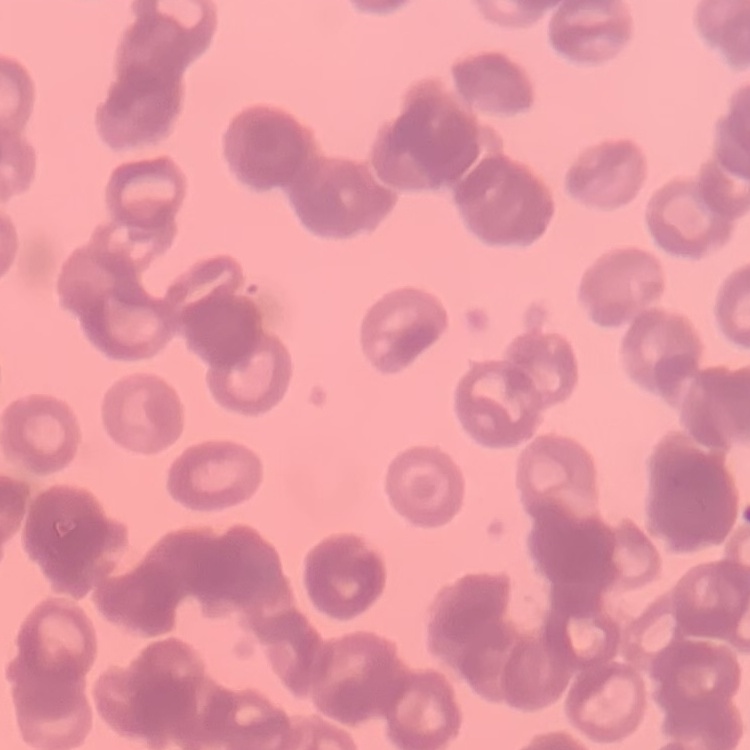

Summary:
  - Red blood cell morphology: rouleaux formation
  - Preparation: thin blood film
  - Image type: square crop of a larger photomicrograph
  - Stain: Field's or Giemsa